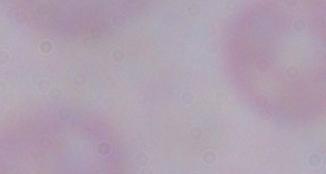

Summary:
  - Identification: trypanosome
  - Magnification: 1000x
  - Modality: photomicrograph